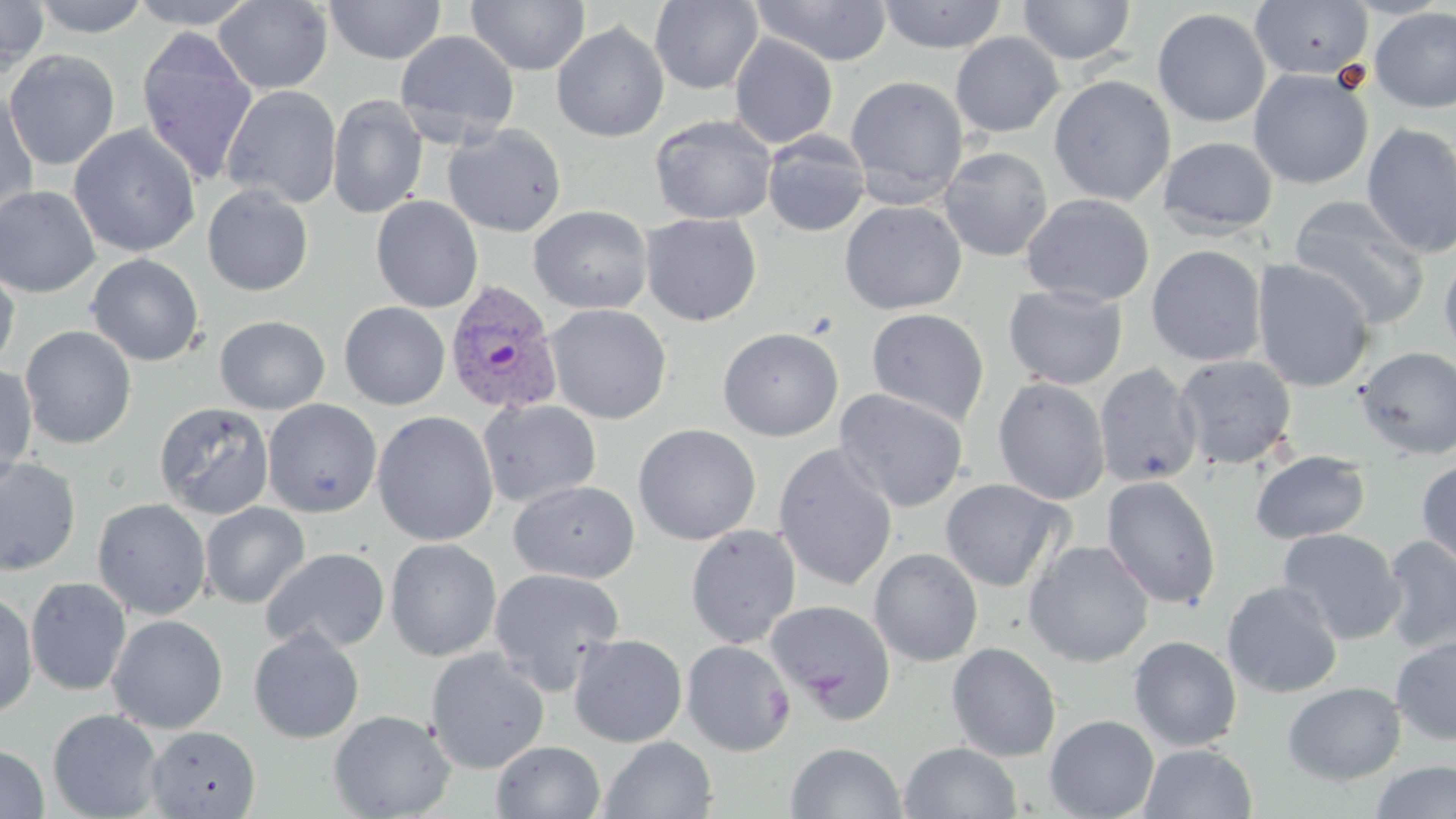
Approximate bounding boxes as named x1/y1/x2/y2 corners in pixels. Plasmodium vivax-infected red blood cell locations: (x1=444, y1=280, x2=563, y2=417). Platelet locations: (x1=762, y1=685, x2=794, y2=725). Uninfected red blood cell locations: (x1=0, y1=0, x2=49, y2=75), (x1=31, y1=0, x2=151, y2=37), (x1=126, y1=0, x2=261, y2=29), (x1=325, y1=0, x2=446, y2=65), (x1=467, y1=0, x2=590, y2=75), (x1=750, y1=0, x2=893, y2=66), (x1=877, y1=0, x2=1008, y2=53), (x1=1017, y1=0, x2=1137, y2=65), (x1=213, y1=1, x2=333, y2=94), (x1=650, y1=1, x2=763, y2=94), (x1=1250, y1=1, x2=1374, y2=81), (x1=1370, y1=7, x2=1456, y2=113), (x1=1152, y1=8, x2=1271, y2=128), (x1=551, y1=22, x2=669, y2=142), (x1=136, y1=27, x2=258, y2=185), (x1=395, y1=30, x2=520, y2=144), (x1=950, y1=32, x2=1064, y2=137), (x1=729, y1=33, x2=838, y2=149), (x1=3, y1=50, x2=121, y2=170), (x1=1248, y1=69, x2=1373, y2=190), (x1=1048, y1=75, x2=1175, y2=206), (x1=845, y1=76, x2=969, y2=206), (x1=221, y1=85, x2=342, y2=209), (x1=0, y1=91, x2=39, y2=222), (x1=327, y1=95, x2=428, y2=219), (x1=649, y1=114, x2=777, y2=225), (x1=1361, y1=122, x2=1456, y2=258), (x1=443, y1=123, x2=567, y2=236), (x1=69, y1=124, x2=201, y2=258), (x1=761, y1=132, x2=871, y2=237), (x1=1158, y1=136, x2=1278, y2=237), (x1=938, y1=147, x2=1054, y2=262), (x1=202, y1=184, x2=314, y2=296), (x1=0, y1=185, x2=101, y2=298), (x1=1021, y1=193, x2=1155, y2=307), (x1=1288, y1=195, x2=1430, y2=330), (x1=371, y1=196, x2=483, y2=313), (x1=839, y1=200, x2=967, y2=315), (x1=528, y1=205, x2=653, y2=314), (x1=640, y1=213, x2=762, y2=326), (x1=1146, y1=245, x2=1267, y2=366), (x1=1439, y1=250, x2=1456, y2=361), (x1=86, y1=254, x2=205, y2=366), (x1=1252, y1=259, x2=1375, y2=392), (x1=0, y1=261, x2=19, y2=372), (x1=1004, y1=285, x2=1127, y2=390), (x1=339, y1=302, x2=451, y2=410), (x1=544, y1=303, x2=673, y2=424), (x1=866, y1=308, x2=989, y2=426), (x1=214, y1=315, x2=330, y2=414), (x1=20, y1=325, x2=137, y2=449), (x1=717, y1=327, x2=844, y2=441), (x1=1356, y1=347, x2=1456, y2=460), (x1=1174, y1=354, x2=1298, y2=470), (x1=0, y1=363, x2=38, y2=485), (x1=1095, y1=363, x2=1202, y2=487), (x1=992, y1=377, x2=1111, y2=505), (x1=834, y1=387, x2=969, y2=513), (x1=262, y1=399, x2=382, y2=518), (x1=478, y1=399, x2=602, y2=507), (x1=154, y1=402, x2=274, y2=519), (x1=372, y1=411, x2=499, y2=546), (x1=633, y1=423, x2=761, y2=545), (x1=772, y1=443, x2=898, y2=592), (x1=1250, y1=450, x2=1371, y2=544), (x1=0, y1=456, x2=81, y2=577), (x1=1416, y1=459, x2=1456, y2=571), (x1=1101, y1=475, x2=1221, y2=609), (x1=939, y1=478, x2=1070, y2=592), (x1=509, y1=480, x2=640, y2=583), (x1=92, y1=498, x2=212, y2=620), (x1=200, y1=501, x2=310, y2=608), (x1=685, y1=524, x2=801, y2=648), (x1=1277, y1=528, x2=1405, y2=644), (x1=1381, y1=535, x2=1456, y2=655), (x1=385, y1=538, x2=502, y2=661), (x1=1023, y1=540, x2=1155, y2=667), (x1=260, y1=547, x2=391, y2=654), (x1=868, y1=547, x2=984, y2=667), (x1=488, y1=568, x2=625, y2=692), (x1=25, y1=577, x2=132, y2=696), (x1=1222, y1=581, x2=1343, y2=699), (x1=0, y1=591, x2=38, y2=721), (x1=766, y1=600, x2=896, y2=721), (x1=107, y1=614, x2=228, y2=733), (x1=248, y1=627, x2=365, y2=744), (x1=568, y1=634, x2=687, y2=747), (x1=1128, y1=635, x2=1242, y2=752), (x1=1391, y1=636, x2=1456, y2=746), (x1=681, y1=640, x2=795, y2=756), (x1=946, y1=642, x2=1061, y2=762), (x1=425, y1=648, x2=549, y2=774), (x1=1282, y1=681, x2=1406, y2=785), (x1=47, y1=709, x2=164, y2=819), (x1=328, y1=709, x2=456, y2=819), (x1=1045, y1=714, x2=1159, y2=819), (x1=146, y1=725, x2=261, y2=818), (x1=598, y1=735, x2=718, y2=819), (x1=492, y1=741, x2=606, y2=819), (x1=785, y1=741, x2=906, y2=819), (x1=900, y1=742, x2=1022, y2=819), (x1=1138, y1=743, x2=1258, y2=819), (x1=1, y1=744, x2=49, y2=819), (x1=1369, y1=760, x2=1456, y2=818). Slide-level diagnosis: Plasmodium vivax. Captured at 1000x magnification. One field of a larger specimen. Image is 1456×819 pixels. Thin blood smear. Light microscopy. May-Grünwald-Giemsa stain.